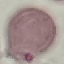

Summary:
  - Malaria status: uninfected
  - Preparation: thin blood smear
  - Stain: Giemsa
  - Capture: smartphone through the microscope eyepiece
  - Image type: cell patch, automatically extracted from a larger field of view and resized to 64 × 64 pixels